Outline each Plasmodium falciparum-infected red blood cell.
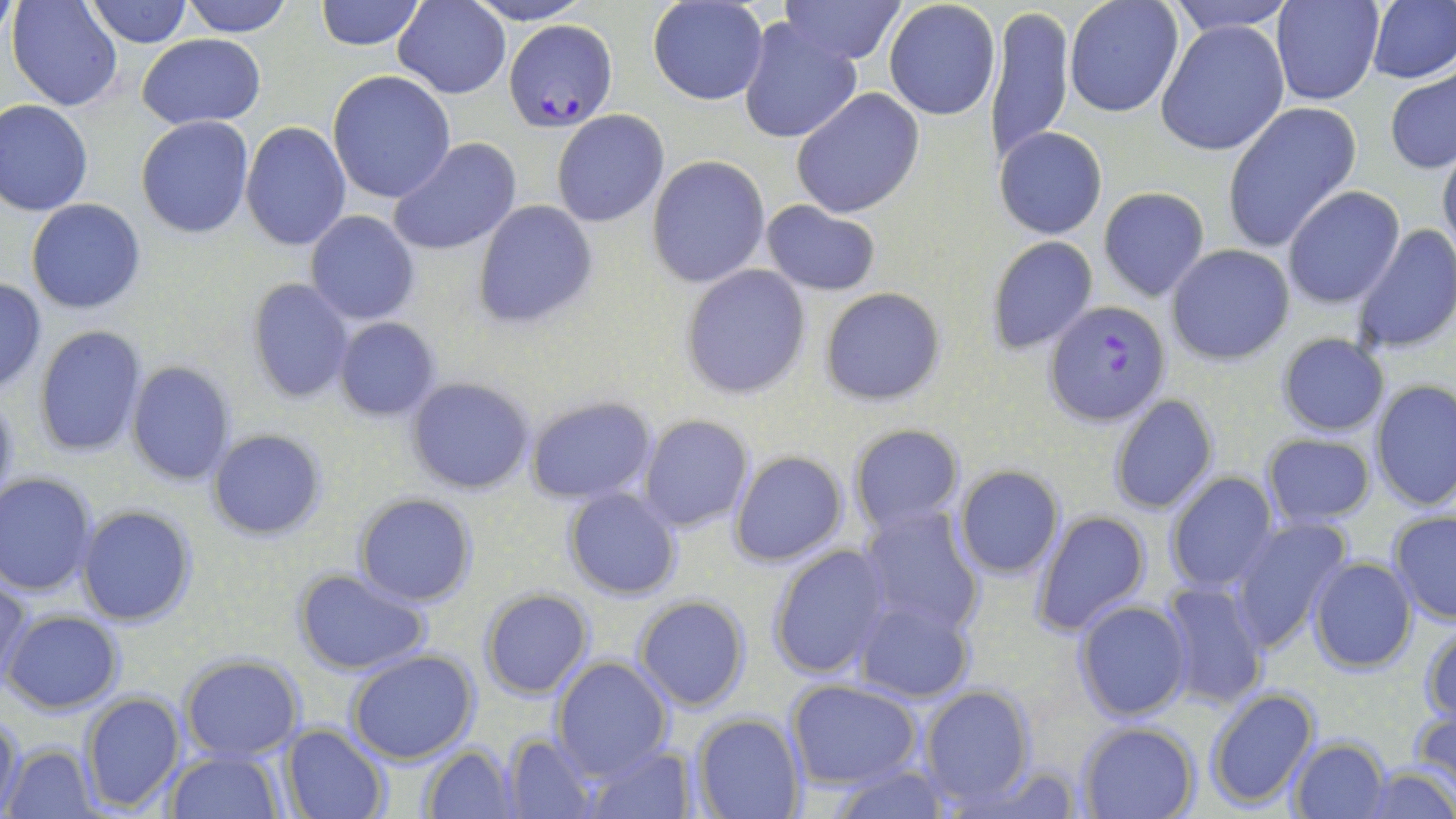

Approximate bounding boxes as [x1, y1, x2, y2] in pixels.
Plasmodium falciparum-infected red blood cells: [504, 20, 616, 133], [1043, 299, 1171, 426].

Summary:
  - Uninfected red blood cell locations: [7, 0, 125, 112], [87, 0, 193, 48], [180, 0, 294, 36], [315, 0, 423, 51], [393, 0, 510, 98], [464, 0, 593, 25], [778, 0, 907, 66], [1064, 0, 1184, 118], [1163, 0, 1295, 35], [1272, 0, 1383, 105], [1365, 0, 1455, 85], [647, 1, 767, 105], [883, 1, 1000, 119], [988, 3, 1074, 167], [737, 16, 861, 145], [1157, 19, 1292, 158], [136, 34, 265, 129], [328, 71, 457, 202], [1384, 71, 1456, 173], [791, 88, 924, 218], [1, 100, 93, 217], [1222, 103, 1360, 252], [552, 111, 670, 227], [135, 116, 254, 238], [241, 120, 352, 252], [993, 127, 1109, 240], [387, 137, 522, 256], [1438, 144, 1456, 262], [646, 155, 772, 288], [1097, 186, 1210, 302], [1281, 186, 1402, 308], [26, 199, 147, 314], [473, 199, 597, 330], [760, 200, 881, 296], [306, 211, 420, 324], [1352, 224, 1456, 355], [264, 231, 384, 380], [984, 235, 1098, 354], [1166, 243, 1295, 366], [680, 264, 812, 399], [0, 276, 47, 394], [246, 278, 354, 404], [818, 286, 946, 406], [333, 318, 441, 422], [33, 326, 147, 458], [1275, 333, 1390, 437], [125, 361, 236, 487], [405, 377, 535, 495], [1370, 381, 1456, 514], [0, 388, 20, 518], [1106, 393, 1220, 516], [524, 394, 659, 505], [637, 413, 754, 533], [847, 422, 967, 536], [206, 427, 327, 540], [1260, 433, 1377, 527], [728, 451, 849, 567], [951, 464, 1066, 578], [1164, 471, 1279, 594], [0, 473, 98, 595], [563, 489, 680, 600], [355, 493, 477, 606], [856, 504, 986, 636], [76, 505, 196, 626], [1030, 509, 1153, 637], [1387, 510, 1456, 626], [1228, 518, 1354, 651], [767, 545, 894, 680], [1307, 557, 1417, 673], [292, 567, 433, 677], [1, 569, 31, 687], [1152, 580, 1269, 708], [479, 589, 594, 698], [849, 595, 975, 703], [633, 597, 749, 712], [1072, 599, 1192, 722], [4, 609, 123, 712], [1420, 620, 1456, 725], [347, 652, 478, 765], [179, 655, 304, 760], [551, 656, 675, 776], [786, 680, 922, 789], [919, 684, 1036, 807], [1205, 686, 1321, 810], [79, 690, 185, 813], [1409, 705, 1456, 802], [0, 714, 24, 813], [690, 715, 806, 819], [1076, 721, 1201, 818], [281, 725, 389, 819], [500, 732, 601, 817], [1287, 738, 1390, 818], [576, 741, 696, 818], [4, 743, 100, 817], [421, 743, 520, 817], [165, 749, 284, 817], [955, 760, 1084, 819], [825, 762, 953, 819], [1359, 765, 1454, 819]
  - Slide-level diagnosis: Plasmodium falciparum
  - Image size: 1456×819 pixels
  - Stain: May-Grünwald-Giemsa
  - Magnification: 1000x
  - Preparation: thin blood film
  - Field of view: one of a larger specimen
  - Modality: light microscopy